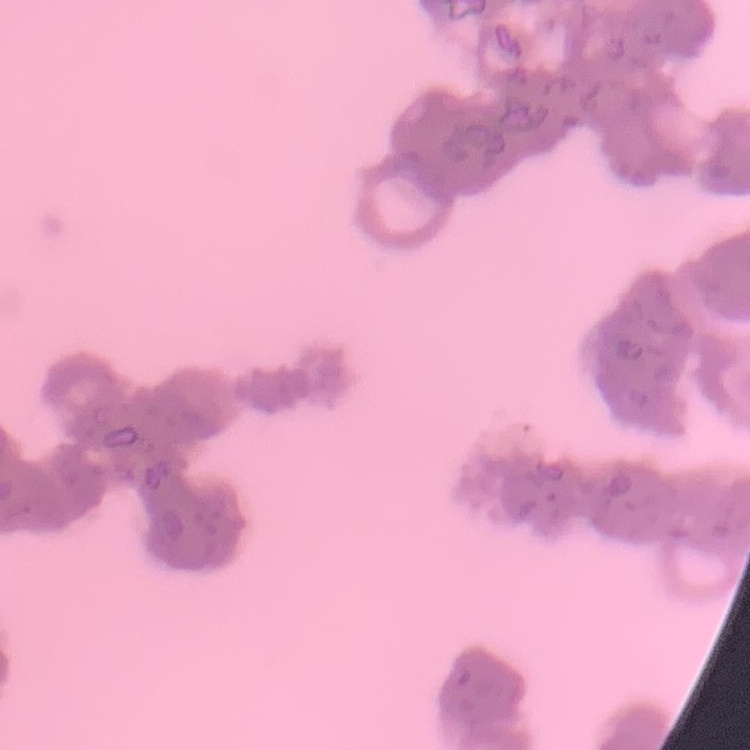
Summary:
  - Red blood cell morphology: rouleaux formation
  - Image type: square crop of a larger photomicrograph
  - Preparation: thin blood smear
  - Stain: Field's or Giemsa